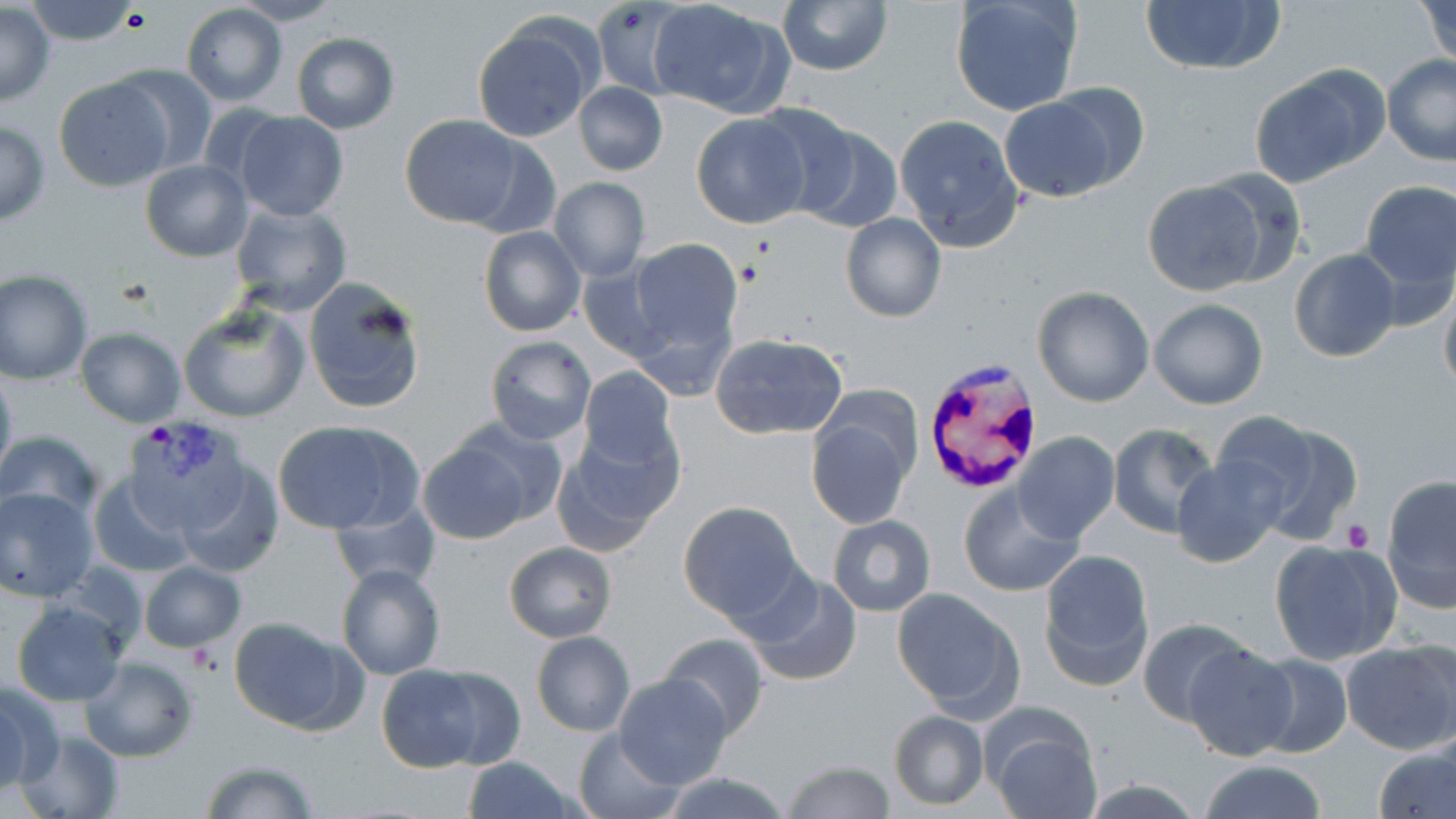
Summary:
  - Coordinate format: approximate bounding boxes as (x1, y1, x2, y2) in pixels
  - Platelet locations: (122, 7, 152, 34), (735, 257, 769, 290), (1345, 518, 1375, 551)
  - Uninfected red blood cell locations: (27, 0, 143, 44), (591, 0, 691, 98), (648, 0, 787, 116), (778, 0, 891, 75), (949, 0, 1082, 116), (1137, 0, 1284, 77), (1418, 0, 1456, 65), (233, 1, 345, 26), (0, 3, 55, 104), (180, 4, 287, 107), (473, 22, 594, 142), (291, 32, 399, 132), (1382, 55, 1456, 166), (109, 66, 220, 172), (1250, 66, 1387, 187), (54, 76, 174, 192), (573, 83, 668, 176), (1047, 84, 1150, 189), (997, 96, 1123, 203), (233, 113, 347, 222), (399, 113, 525, 229), (690, 113, 812, 229), (776, 115, 905, 229), (893, 115, 1025, 252), (0, 119, 50, 227), (462, 136, 562, 239), (140, 160, 252, 261), (1195, 168, 1310, 285), (548, 177, 650, 280), (1139, 180, 1271, 298), (1360, 180, 1455, 291), (228, 202, 353, 317), (840, 212, 947, 322), (478, 226, 586, 337), (628, 238, 743, 360), (1289, 247, 1402, 363), (576, 265, 670, 363), (0, 271, 93, 384), (303, 276, 426, 416), (1438, 285, 1456, 399), (1031, 287, 1154, 407), (1148, 298, 1268, 409), (178, 304, 310, 424), (75, 327, 186, 426), (712, 334, 847, 441), (485, 336, 596, 446), (0, 363, 17, 490), (580, 366, 678, 470), (806, 402, 918, 529), (1217, 414, 1360, 544), (270, 421, 417, 533), (451, 421, 566, 528), (1108, 423, 1218, 539), (553, 431, 680, 557), (1, 432, 103, 526), (1014, 432, 1120, 543), (415, 436, 535, 546), (1172, 456, 1286, 569), (175, 463, 282, 578), (87, 474, 194, 579), (1381, 477, 1456, 613), (957, 486, 1086, 597), (1, 487, 99, 603), (328, 500, 441, 591), (678, 500, 803, 622), (826, 515, 936, 616), (1269, 539, 1402, 667), (503, 541, 616, 643), (1038, 548, 1155, 690), (139, 561, 248, 653), (335, 563, 446, 680), (743, 571, 863, 687), (889, 587, 1023, 716), (12, 600, 126, 707), (229, 618, 354, 732), (1137, 618, 1251, 723), (531, 631, 634, 736), (658, 633, 768, 737), (1341, 640, 1456, 754), (1182, 643, 1300, 760), (1250, 654, 1352, 757), (79, 657, 198, 763), (375, 665, 495, 774), (427, 666, 525, 769), (614, 674, 733, 789), (1, 684, 55, 795), (0, 691, 28, 794), (889, 711, 989, 810), (991, 721, 1102, 819), (16, 727, 124, 819), (572, 730, 683, 817), (1375, 745, 1455, 819), (461, 757, 577, 818), (783, 758, 895, 818), (199, 759, 320, 818), (1197, 760, 1328, 818), (656, 769, 791, 819), (1080, 780, 1207, 817)
  - Plasmodium vivax-infected red blood cell locations: (927, 355, 1041, 490), (120, 417, 256, 539)
  - Slide-level diagnosis: Plasmodium vivax
  - Image size: 1456×819 pixels
  - Field of view: single
  - Magnification: 1000x
  - Stain: May-Grünwald-Giemsa
  - Preparation: thin blood smear
  - Modality: optical microscopy